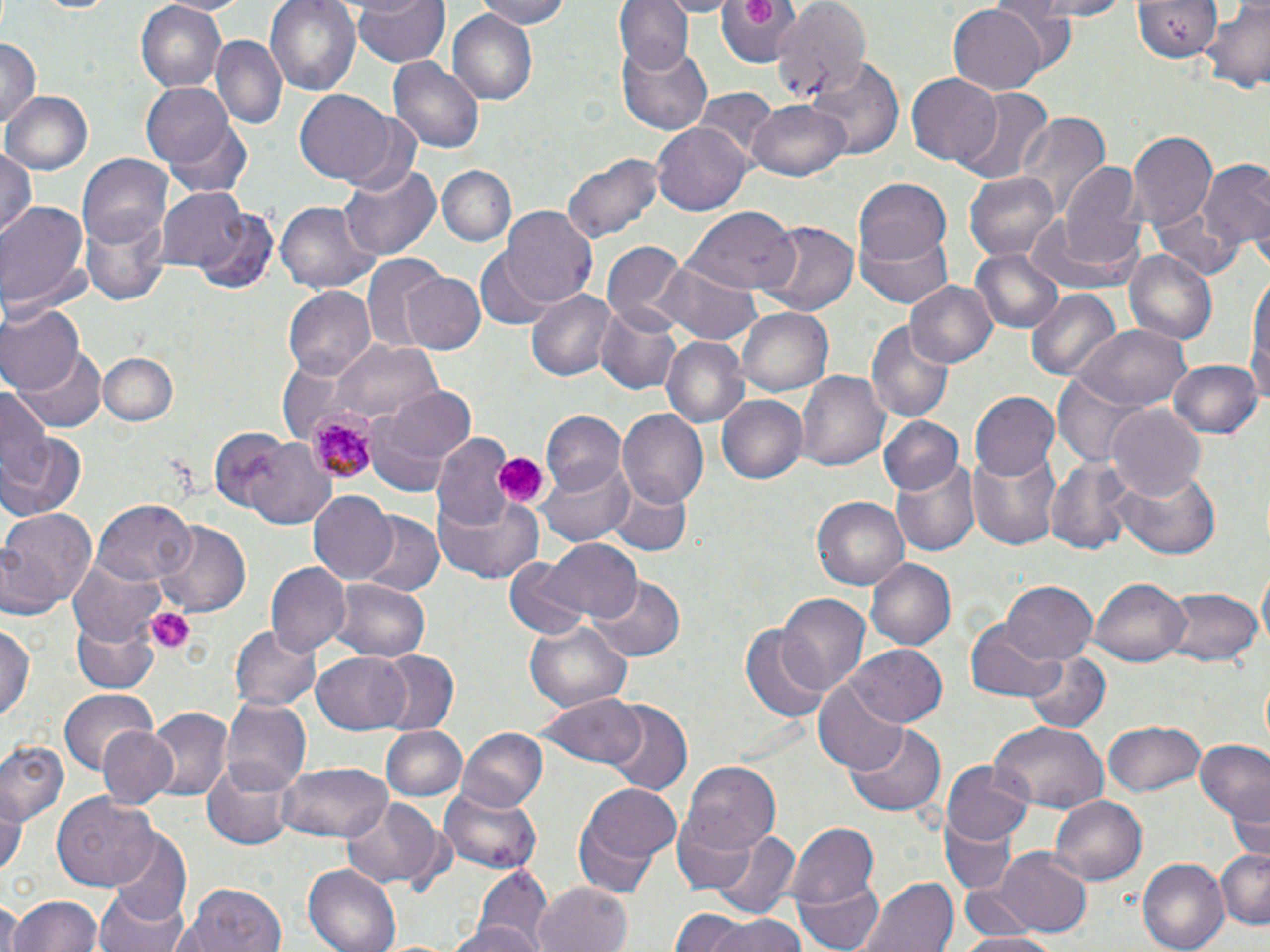
Approximate bounding boxes as [x1, y1, x2, y2] in pixels. Plasmodium malariae-infected red blood cell locations: [305, 406, 380, 479]. Platelet locations: [742, 0, 778, 27], [489, 449, 549, 509], [143, 605, 195, 655]. Uninfected red blood cell locations: [135, 0, 228, 89], [156, 0, 251, 17], [265, 0, 360, 98], [353, 0, 449, 69], [472, 0, 574, 29], [616, 0, 693, 73], [714, 0, 799, 70], [769, 0, 869, 106], [1021, 0, 1134, 20], [1132, 1, 1224, 59], [1200, 2, 1270, 91], [947, 4, 1045, 94], [449, 11, 538, 105], [210, 35, 286, 131], [618, 35, 716, 134], [0, 38, 41, 133], [803, 56, 906, 161], [389, 58, 484, 156], [907, 73, 1003, 165], [140, 83, 235, 169], [954, 89, 1054, 185], [694, 90, 780, 169], [4, 91, 91, 177], [295, 91, 395, 184], [747, 100, 853, 182], [328, 105, 426, 195], [1016, 111, 1108, 216], [654, 121, 752, 216], [167, 122, 253, 199], [1127, 132, 1217, 228], [0, 146, 38, 242], [563, 153, 662, 244], [77, 154, 174, 252], [1192, 159, 1270, 263], [341, 161, 438, 261], [1057, 164, 1149, 272], [439, 166, 516, 246], [963, 169, 1060, 262], [852, 177, 949, 271], [157, 186, 259, 276], [276, 200, 373, 294], [0, 201, 90, 319], [190, 206, 277, 293], [501, 208, 597, 305], [683, 209, 796, 297], [83, 214, 170, 306], [1026, 220, 1141, 297], [760, 221, 858, 316], [854, 221, 957, 310], [601, 240, 688, 334], [972, 249, 1063, 334], [1123, 249, 1219, 347], [474, 250, 556, 331], [360, 256, 449, 351], [654, 263, 761, 346], [400, 272, 485, 353], [1246, 276, 1269, 409], [905, 278, 997, 369], [1024, 285, 1121, 381], [282, 286, 374, 380], [527, 292, 619, 382], [0, 303, 83, 396], [596, 308, 683, 396], [737, 308, 833, 395], [866, 319, 954, 421], [1073, 326, 1190, 410], [661, 335, 748, 429], [329, 339, 441, 424], [16, 343, 107, 431], [98, 353, 178, 428], [1169, 357, 1262, 438], [799, 371, 889, 471], [1054, 377, 1149, 467], [0, 380, 48, 491], [368, 385, 479, 486], [970, 391, 1063, 483], [717, 394, 810, 484], [1107, 403, 1206, 500], [617, 410, 709, 508], [541, 412, 624, 496], [877, 417, 965, 496], [205, 427, 293, 511], [2, 432, 87, 522], [433, 434, 521, 533], [246, 442, 338, 530], [968, 447, 1065, 551], [540, 456, 635, 546], [1044, 457, 1139, 555], [893, 461, 979, 557], [1114, 466, 1220, 559], [608, 480, 691, 557], [309, 492, 397, 583], [433, 494, 544, 585], [812, 496, 910, 591], [92, 502, 195, 584], [0, 506, 97, 618], [356, 512, 443, 597], [153, 522, 249, 616], [537, 540, 640, 624], [69, 554, 167, 644], [866, 556, 956, 650], [504, 558, 596, 641], [266, 563, 352, 658], [1257, 564, 1269, 650], [590, 576, 685, 661], [1000, 579, 1098, 665], [1092, 579, 1189, 666], [328, 581, 432, 663], [1163, 587, 1261, 666], [775, 592, 870, 698], [73, 613, 160, 692], [523, 618, 631, 712], [964, 619, 1063, 703], [1, 622, 33, 725], [231, 623, 321, 712], [741, 625, 832, 725], [849, 644, 947, 726], [374, 650, 459, 735], [1023, 651, 1111, 736], [313, 652, 413, 732], [812, 678, 910, 776], [60, 688, 158, 775], [536, 695, 647, 771], [221, 698, 310, 791], [603, 702, 691, 793], [146, 708, 232, 799], [990, 720, 1110, 813], [1102, 720, 1206, 798], [847, 723, 947, 816], [97, 724, 178, 810], [382, 725, 465, 803], [457, 727, 548, 814], [1193, 737, 1270, 823], [0, 740, 67, 826], [201, 756, 297, 849], [278, 760, 394, 843], [680, 761, 783, 854], [941, 763, 1037, 848], [576, 781, 682, 882], [1225, 783, 1270, 863], [440, 787, 541, 873], [0, 793, 24, 880], [53, 793, 159, 889], [1050, 796, 1146, 884], [342, 797, 443, 889], [671, 812, 768, 894], [937, 817, 1017, 898], [787, 823, 880, 911], [706, 826, 801, 920], [107, 835, 192, 929], [985, 849, 1094, 938], [1215, 849, 1269, 928], [1137, 856, 1229, 952], [303, 864, 400, 952], [468, 867, 550, 949], [793, 873, 885, 952], [860, 878, 959, 952], [532, 881, 635, 952], [176, 882, 289, 952], [954, 886, 1055, 944], [94, 889, 189, 952], [10, 893, 103, 952], [0, 901, 22, 952], [670, 909, 765, 951], [450, 913, 541, 950], [704, 916, 810, 952], [955, 931, 1060, 952]. Slide-level diagnosis: Plasmodium malariae. May-Grünwald-Giemsa-stained preparation. One field of a larger specimen. Captured at 1000x magnification. Thin blood film. Light microscopy. Image is 1270×952 pixels.